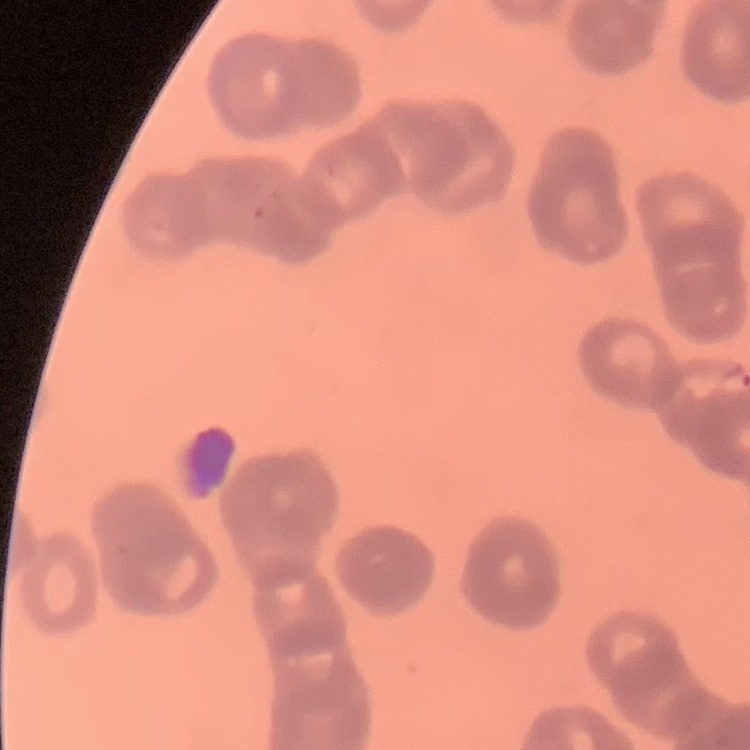

The red blood cells show rouleaux formation. Stained with either Field's or Giemsa. One tile cut from a larger photomicrograph. Thin peripheral smear.